Locate and identify every blood parasite.
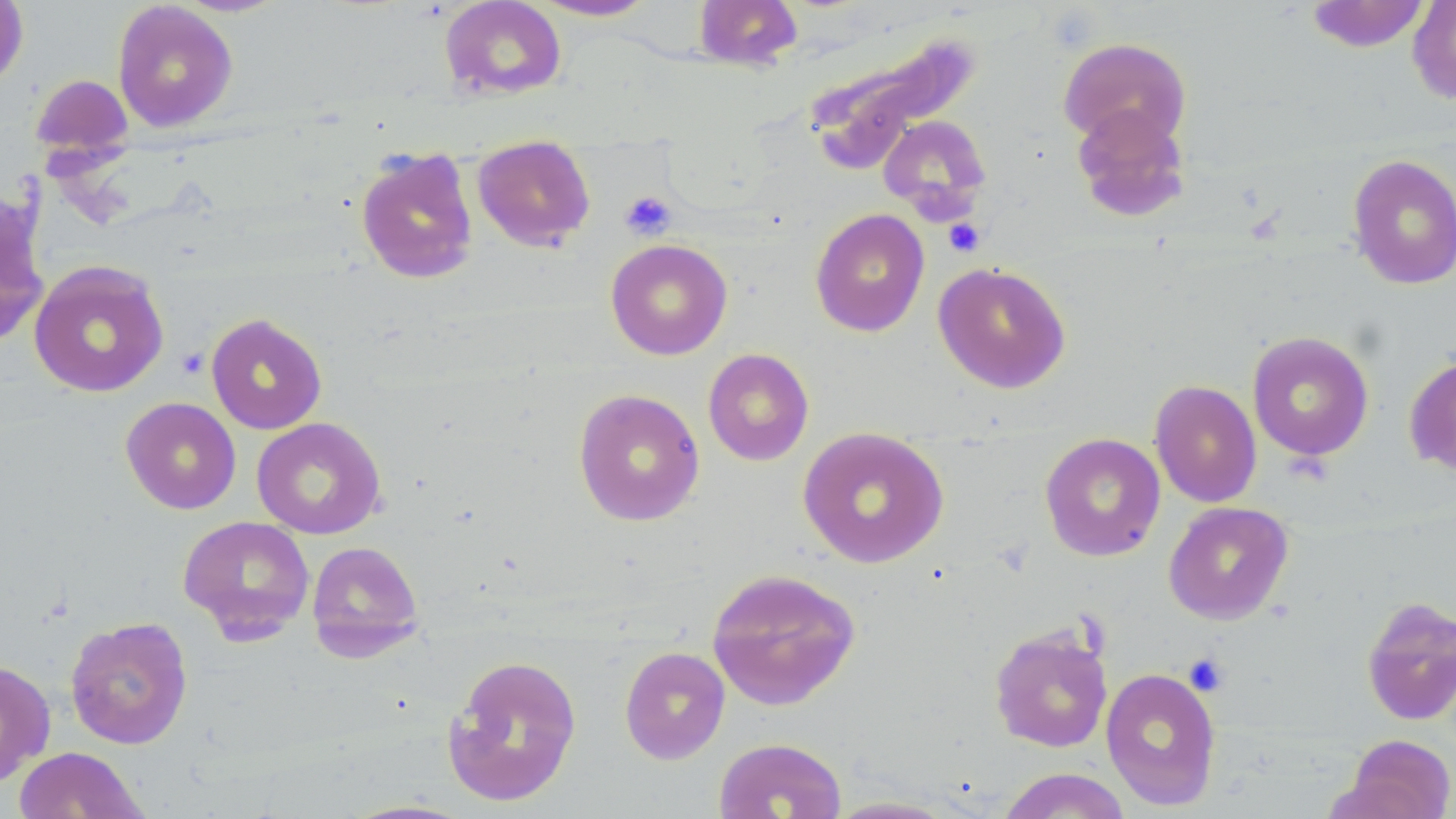
No blood parasites seen.

Approximate bounding boxes as (x1, y1, x2, y2) in pixels. Platelet locations: (619, 190, 677, 241), (942, 218, 984, 257), (1183, 653, 1229, 696). Uninfected red blood cell locations: (439, 0, 567, 101), (693, 0, 802, 71), (1305, 0, 1430, 53), (1407, 0, 1456, 105), (0, 1, 28, 91), (530, 1, 659, 21), (112, 2, 238, 132), (802, 30, 982, 174), (1057, 37, 1193, 152), (31, 73, 132, 158), (1070, 104, 1192, 222), (877, 114, 992, 221), (472, 135, 596, 251), (357, 141, 596, 265), (355, 146, 479, 284), (1346, 154, 1456, 290), (0, 190, 49, 349), (810, 208, 930, 337), (605, 239, 733, 360), (28, 260, 169, 398), (932, 261, 1072, 393), (205, 313, 328, 434), (1246, 331, 1374, 461), (702, 348, 814, 466), (1403, 353, 1456, 476), (1149, 379, 1262, 508), (573, 387, 705, 527), (120, 397, 242, 514), (251, 417, 386, 539), (798, 426, 949, 568), (1039, 432, 1166, 562), (1163, 501, 1293, 624), (177, 514, 315, 643), (306, 540, 424, 661), (706, 567, 862, 711), (1361, 595, 1456, 726), (65, 616, 193, 749), (989, 624, 1114, 753), (619, 646, 730, 764), (442, 653, 583, 807), (0, 659, 55, 788), (1100, 667, 1222, 810), (1337, 734, 1456, 819), (713, 737, 847, 819), (13, 746, 149, 819), (996, 767, 1131, 818), (820, 795, 962, 818). Slide-level diagnosis: no evidence of blood parasites. Image is 1456×819 pixels. Thin blood film. May-Grünwald-Giemsa stain. Single field of view. Captured at 1000x magnification. Light microscopy.